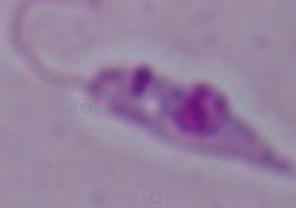

identification = Leishmania
magnification = 1000x
modality = photomicrograph